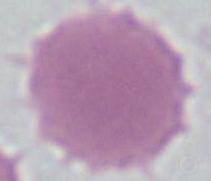 Captured at 1000x magnification. An erythrocyte is seen. Micrograph.